Classify this cell by malaria status.
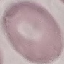
It is uninfected.

Thin blood film. Automatically extracted cell patch, resized to 64 × 64 pixels. Giemsa-stained preparation. Photographed with a smartphone camera at the microscope eyepiece.